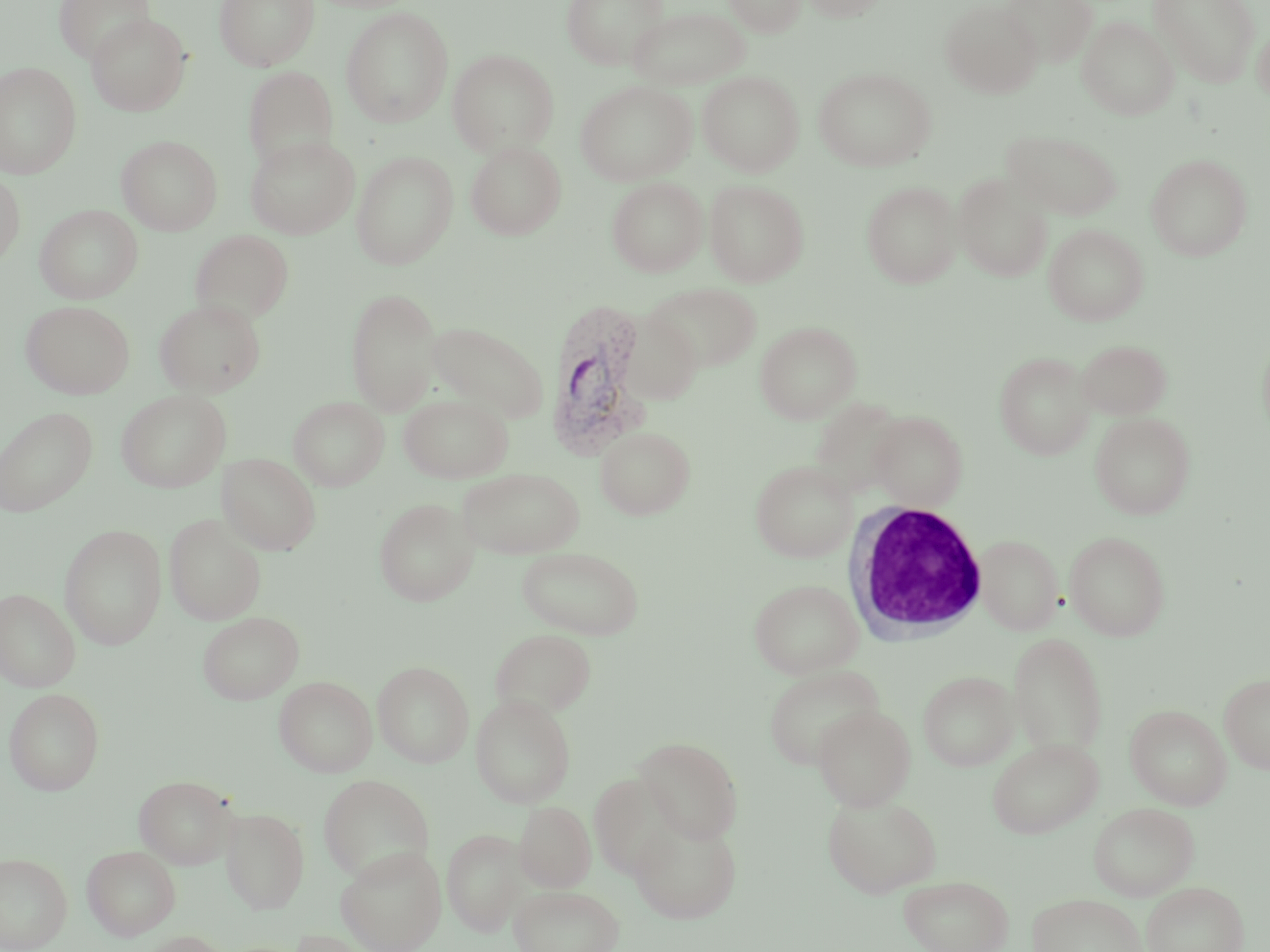

Summary:
  - Coordinate format: approximate bounding boxes as [x1, y1, x2, y2] in pixels
  - Plasmodium vivax-infected red blood cell locations: [542, 300, 653, 460]
  - White blood cell locations: [843, 501, 991, 642]
  - Uninfected red blood cell locations: [54, 0, 155, 65], [214, 0, 320, 70], [560, 0, 670, 69], [722, 0, 807, 36], [802, 0, 888, 22], [940, 0, 1043, 98], [1151, 0, 1261, 87], [1001, 1, 1098, 68], [629, 6, 751, 90], [340, 7, 454, 127], [86, 13, 191, 116], [1077, 15, 1179, 120], [1252, 17, 1270, 104], [447, 49, 559, 157], [0, 62, 82, 178], [243, 67, 339, 173], [813, 67, 936, 172], [698, 70, 805, 176], [575, 80, 697, 186], [1002, 128, 1123, 221], [245, 134, 360, 238], [117, 135, 222, 235], [465, 140, 567, 240], [351, 151, 458, 269], [1147, 153, 1253, 261], [0, 172, 24, 269], [954, 173, 1053, 282], [607, 177, 708, 277], [704, 179, 809, 287], [861, 181, 963, 288], [35, 205, 143, 304], [1043, 223, 1148, 325], [190, 230, 294, 325], [645, 282, 762, 373], [345, 290, 442, 414], [154, 298, 266, 397], [22, 300, 135, 399], [427, 321, 548, 422], [754, 321, 862, 423], [1076, 339, 1171, 419], [994, 351, 1095, 459], [116, 389, 231, 493], [399, 394, 513, 483], [288, 396, 389, 490], [809, 396, 908, 500], [0, 406, 97, 517], [868, 411, 968, 511], [1089, 412, 1196, 519], [595, 425, 696, 520], [218, 452, 321, 555], [750, 460, 858, 562], [456, 467, 585, 559], [373, 498, 479, 606], [164, 514, 267, 625], [59, 524, 166, 649], [1064, 530, 1171, 641], [973, 534, 1064, 635], [516, 545, 644, 639], [749, 578, 864, 679], [0, 588, 80, 692], [197, 611, 304, 704], [490, 628, 597, 718], [1007, 632, 1108, 759], [372, 661, 474, 767], [762, 665, 884, 770], [918, 670, 1019, 771], [1219, 672, 1270, 775], [274, 675, 377, 777], [3, 688, 104, 795], [470, 694, 576, 807], [813, 704, 916, 811], [1125, 704, 1233, 810], [635, 737, 743, 843], [988, 738, 1103, 838], [589, 770, 682, 880], [133, 774, 238, 869], [318, 774, 434, 883], [822, 795, 943, 897], [515, 801, 596, 893], [1088, 802, 1199, 900], [220, 806, 309, 913], [629, 817, 742, 923], [442, 828, 527, 935], [81, 845, 181, 940], [336, 846, 447, 952], [0, 852, 72, 951], [898, 874, 1014, 952], [1140, 881, 1249, 952], [508, 884, 624, 952], [1027, 893, 1148, 952], [136, 931, 232, 952]
  - Slide-level diagnosis: Plasmodium vivax
  - Modality: optical microscopy
  - Stain: May-Grünwald-Giemsa
  - Preparation: thin blood smear
  - Field of view: single
  - Magnification: 1000x
  - Image size: 1270×952 pixels